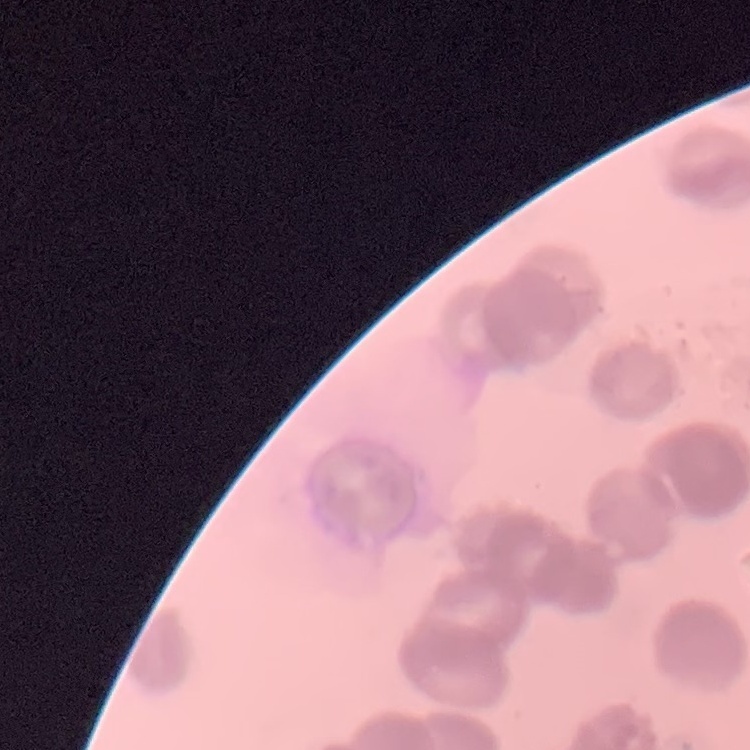
{
  "erythrocyte_morphology": "rouleaux formation",
  "image_type": "square crop of a larger photomicrograph",
  "stain": "Field's or Giemsa",
  "preparation": "thin blood film"
}